Locate and identify every blood parasite.
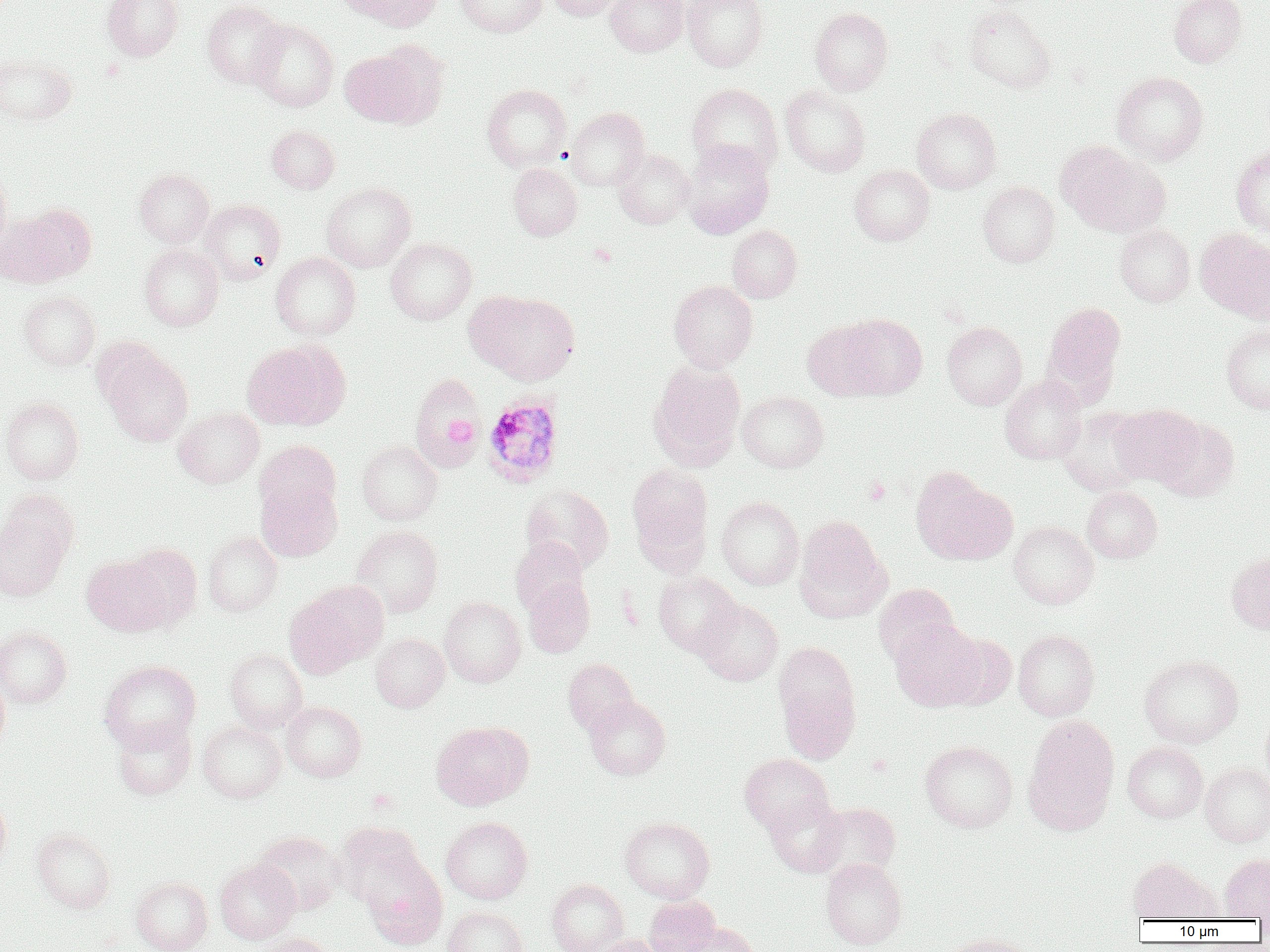
Approximate bounding boxes as named x1/y1/x2/y2 corners in pixels.
Plasmodium ovale-infected red blood cells: (x1=482, y1=393, x2=564, y2=488).
No Plasmodium falciparum, Plasmodium malariae, Plasmodium vivax, Babesia divergens, or Trypanosoma brucei observed.

slide-level diagnosis = Plasmodium ovale
preparation = thin blood film
field of view = one of a larger specimen
modality = light microscopy
uninfected red blood cell locations = approximate bounding boxes as named x1/y1/x2/y2 corners in pixels: (x1=102, y1=0, x2=184, y2=62), (x1=341, y1=0, x2=442, y2=32), (x1=456, y1=0, x2=548, y2=37), (x1=546, y1=0, x2=626, y2=21), (x1=604, y1=0, x2=688, y2=56), (x1=682, y1=0, x2=768, y2=71), (x1=1169, y1=0, x2=1247, y2=66), (x1=202, y1=1, x2=288, y2=88), (x1=963, y1=5, x2=1056, y2=93), (x1=809, y1=8, x2=893, y2=95), (x1=249, y1=19, x2=339, y2=111), (x1=338, y1=46, x2=434, y2=128), (x1=0, y1=53, x2=77, y2=126), (x1=1111, y1=71, x2=1209, y2=165), (x1=688, y1=83, x2=782, y2=176), (x1=481, y1=84, x2=571, y2=171), (x1=780, y1=85, x2=870, y2=176), (x1=566, y1=107, x2=650, y2=190), (x1=912, y1=107, x2=1001, y2=194), (x1=267, y1=125, x2=339, y2=193), (x1=681, y1=141, x2=774, y2=238), (x1=1059, y1=145, x2=1170, y2=237), (x1=1231, y1=146, x2=1270, y2=235), (x1=613, y1=149, x2=695, y2=229), (x1=508, y1=163, x2=582, y2=240), (x1=0, y1=164, x2=12, y2=257), (x1=849, y1=165, x2=934, y2=245), (x1=134, y1=168, x2=214, y2=246), (x1=978, y1=181, x2=1060, y2=267), (x1=321, y1=182, x2=416, y2=272), (x1=200, y1=199, x2=286, y2=284), (x1=16, y1=203, x2=96, y2=283), (x1=0, y1=212, x2=66, y2=287), (x1=1114, y1=224, x2=1195, y2=306), (x1=726, y1=225, x2=803, y2=302), (x1=1195, y1=228, x2=1270, y2=321), (x1=386, y1=238, x2=476, y2=325), (x1=139, y1=244, x2=223, y2=331), (x1=271, y1=252, x2=360, y2=340), (x1=669, y1=280, x2=758, y2=371), (x1=18, y1=291, x2=101, y2=370), (x1=468, y1=291, x2=580, y2=384), (x1=1042, y1=301, x2=1126, y2=400), (x1=838, y1=314, x2=927, y2=399), (x1=803, y1=320, x2=886, y2=399), (x1=942, y1=322, x2=1027, y2=410), (x1=1221, y1=323, x2=1270, y2=414), (x1=242, y1=340, x2=350, y2=430), (x1=101, y1=349, x2=194, y2=446), (x1=647, y1=361, x2=745, y2=471), (x1=408, y1=372, x2=485, y2=470), (x1=1000, y1=374, x2=1086, y2=464), (x1=737, y1=391, x2=828, y2=472), (x1=1, y1=397, x2=84, y2=484), (x1=1110, y1=404, x2=1203, y2=485), (x1=173, y1=407, x2=264, y2=488), (x1=1057, y1=407, x2=1150, y2=496), (x1=1155, y1=417, x2=1239, y2=501), (x1=255, y1=440, x2=341, y2=519), (x1=356, y1=440, x2=442, y2=525), (x1=627, y1=464, x2=713, y2=566), (x1=914, y1=473, x2=1017, y2=565), (x1=256, y1=479, x2=342, y2=561), (x1=520, y1=484, x2=613, y2=573), (x1=1082, y1=486, x2=1162, y2=562), (x1=0, y1=495, x2=76, y2=600), (x1=716, y1=496, x2=803, y2=589), (x1=794, y1=516, x2=891, y2=622), (x1=1009, y1=521, x2=1098, y2=608), (x1=351, y1=526, x2=443, y2=617), (x1=202, y1=530, x2=283, y2=617), (x1=510, y1=537, x2=589, y2=615), (x1=121, y1=544, x2=202, y2=629), (x1=1226, y1=550, x2=1270, y2=635), (x1=82, y1=555, x2=173, y2=636), (x1=653, y1=570, x2=742, y2=656), (x1=523, y1=578, x2=595, y2=657), (x1=286, y1=584, x2=382, y2=674), (x1=873, y1=584, x2=959, y2=665), (x1=439, y1=597, x2=526, y2=686), (x1=694, y1=600, x2=783, y2=685), (x1=890, y1=619, x2=985, y2=711), (x1=0, y1=626, x2=72, y2=707), (x1=1013, y1=629, x2=1099, y2=720), (x1=371, y1=634, x2=449, y2=711), (x1=943, y1=634, x2=1016, y2=709), (x1=775, y1=642, x2=861, y2=759), (x1=224, y1=649, x2=308, y2=733), (x1=1139, y1=654, x2=1243, y2=747), (x1=564, y1=659, x2=638, y2=734), (x1=100, y1=660, x2=201, y2=750), (x1=0, y1=674, x2=10, y2=753), (x1=584, y1=695, x2=670, y2=779), (x1=281, y1=701, x2=366, y2=782), (x1=1261, y1=711, x2=1270, y2=789), (x1=112, y1=716, x2=196, y2=799), (x1=1022, y1=716, x2=1120, y2=835), (x1=197, y1=721, x2=286, y2=802), (x1=431, y1=721, x2=533, y2=810), (x1=920, y1=740, x2=1017, y2=833), (x1=1122, y1=742, x2=1208, y2=822), (x1=739, y1=753, x2=834, y2=833), (x1=1200, y1=763, x2=1270, y2=846), (x1=0, y1=794, x2=12, y2=874), (x1=765, y1=795, x2=848, y2=876), (x1=812, y1=802, x2=901, y2=880), (x1=440, y1=817, x2=533, y2=904), (x1=619, y1=817, x2=715, y2=903), (x1=335, y1=821, x2=425, y2=907), (x1=33, y1=828, x2=115, y2=913), (x1=253, y1=831, x2=346, y2=915), (x1=1219, y1=853, x2=1270, y2=921), (x1=360, y1=855, x2=447, y2=950), (x1=1127, y1=857, x2=1218, y2=921), (x1=821, y1=858, x2=907, y2=949), (x1=215, y1=860, x2=300, y2=943), (x1=131, y1=876, x2=212, y2=952), (x1=547, y1=879, x2=628, y2=952), (x1=644, y1=895, x2=720, y2=952), (x1=442, y1=906, x2=528, y2=952), (x1=678, y1=922, x2=760, y2=952), (x1=938, y1=932, x2=1035, y2=952), (x1=251, y1=934, x2=335, y2=952), (x1=589, y1=934, x2=668, y2=952)
platelet locations = approximate bounding boxes as named x1/y1/x2/y2 corners in pixels: (x1=589, y1=243, x2=617, y2=267), (x1=445, y1=418, x2=478, y2=447), (x1=864, y1=477, x2=889, y2=506)
image size = 1270×952 pixels
magnification = 1000x